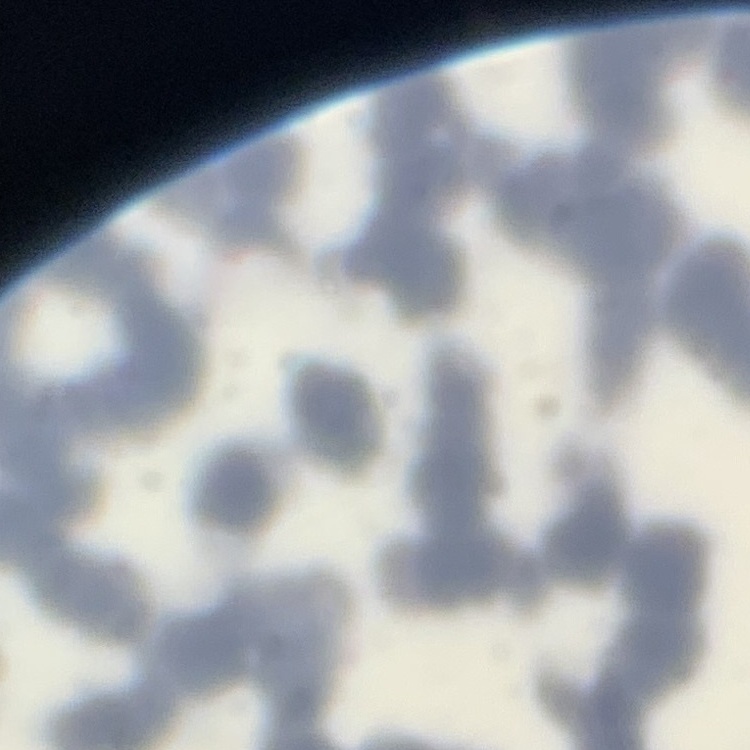
red blood cell morphology = rouleaux formation
stain = Field's or Giemsa
image type = square crop of a larger photomicrograph
preparation = thin blood film